State which parasite is depicted.
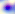
This is Toxoplasma gondii.

Photomicrograph. Captured at 400x magnification.